Report the malaria status.
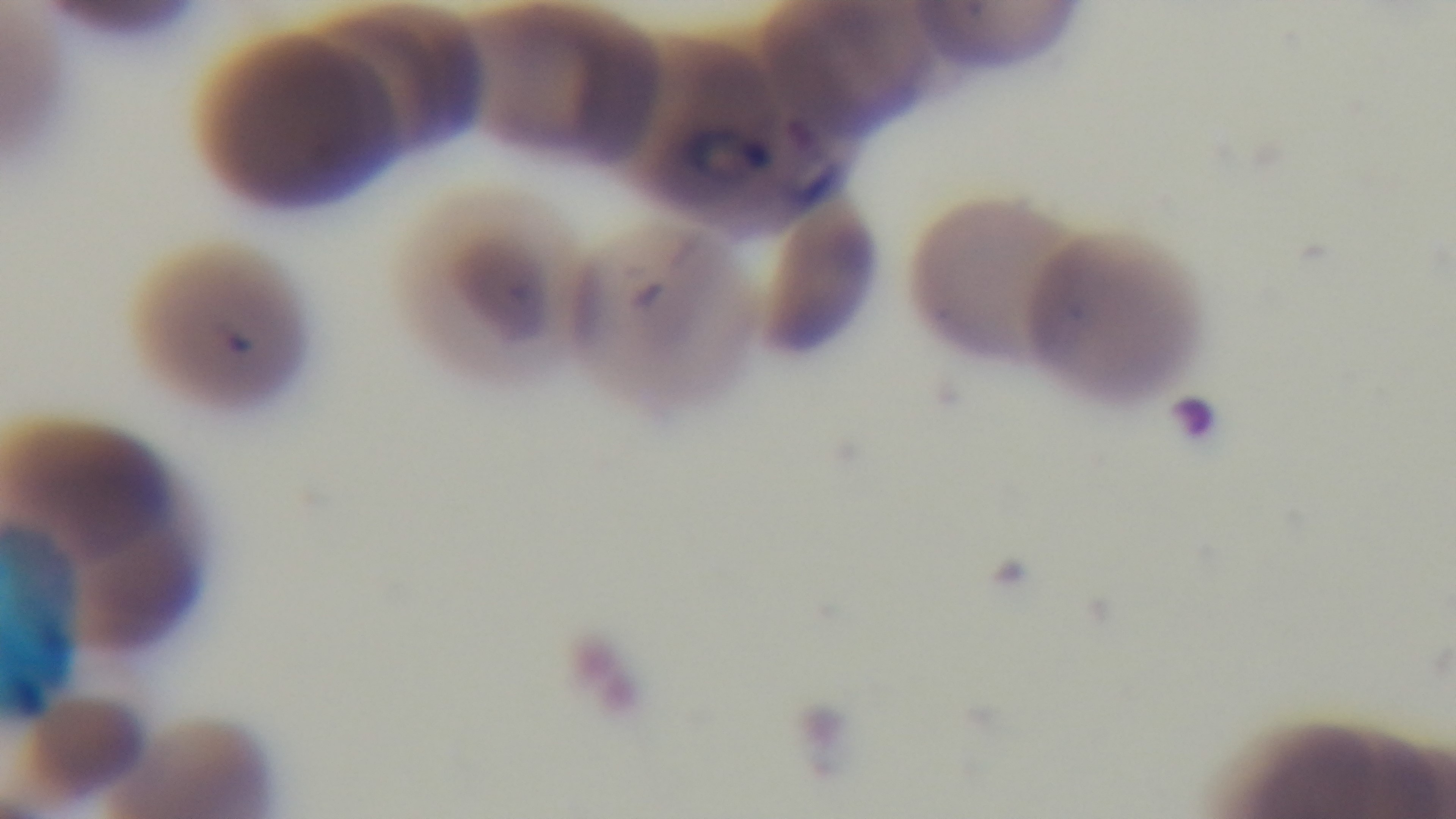

Positive.

Summary:
  - Stain: Giemsa
  - Modality: light microscopy
  - Preparation: thin smear
  - Capture: mounted 4K digital camera
  - Objective: 100x oil immersion
  - Field of view: single